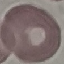

malaria status = uninfected
stain = Giemsa
preparation = thin blood smear
image type = cell patch, automatically extracted from a larger field of view and resized to 64 × 64 pixels
capture = smartphone through the microscope eyepiece